Assess this cell for malaria.
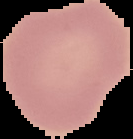

Uninfected.

Image is 133×139 pixels. Segmented cell region on a black background. From a thin blood film.